Identify the parasite.
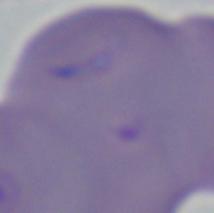

This is Babesia.

Photomicrograph. Captured at 1000x magnification.